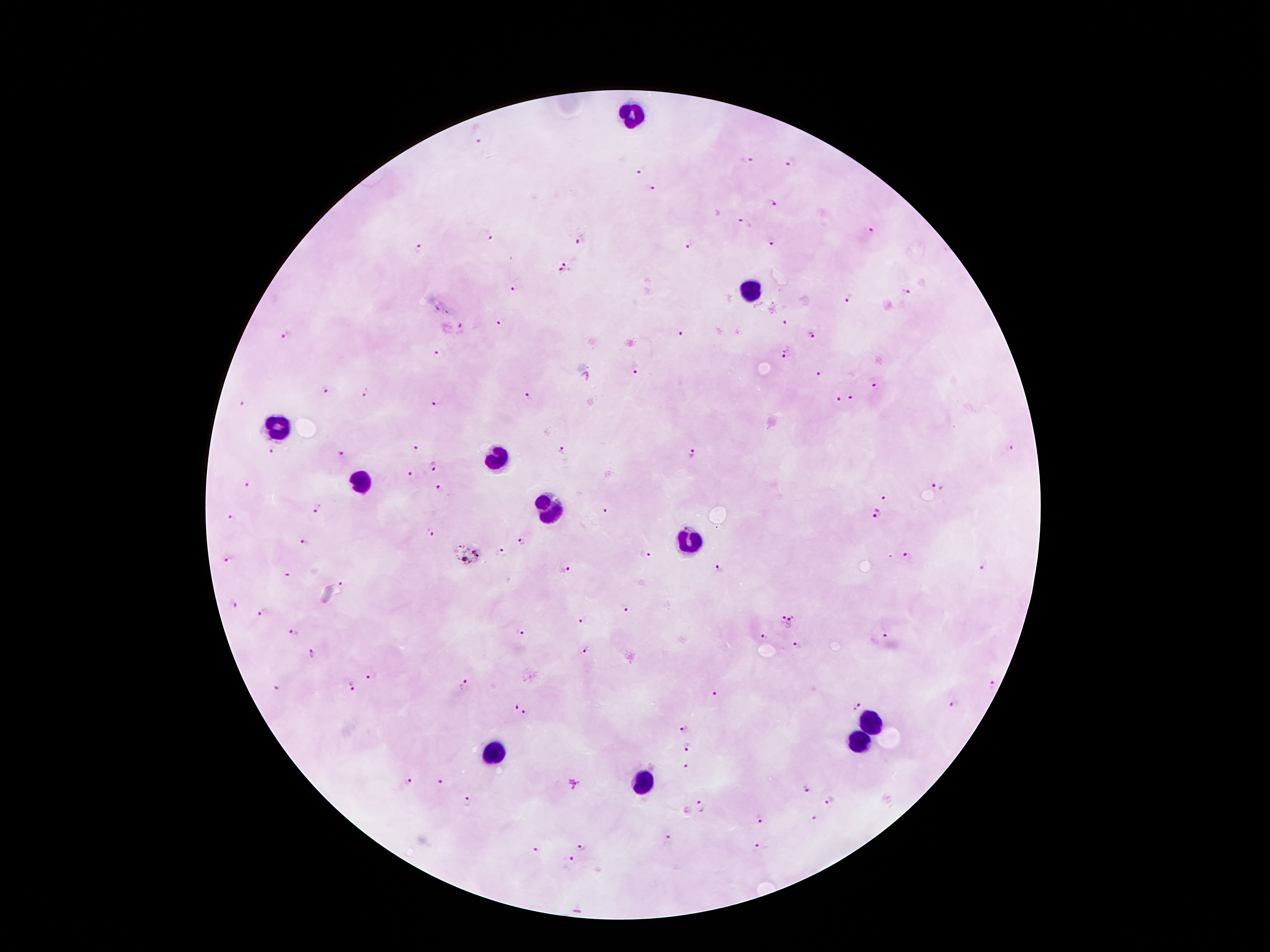

Approximate centers as [x, y] in pixels.
Summary:
  - Plasmodium parasite locations: [480, 142], [746, 161], [793, 162], [642, 170], [652, 189], [774, 203], [745, 224], [870, 230], [581, 239], [490, 240], [771, 241], [691, 245], [418, 248], [566, 262], [560, 273], [516, 288], [906, 293], [850, 301], [502, 322], [783, 323], [461, 326], [680, 333], [286, 336], [811, 336], [435, 352], [787, 353], [636, 368], [821, 376], [874, 385], [326, 387], [365, 393], [529, 396], [852, 397], [839, 401], [435, 402], [242, 404], [417, 447], [1012, 448], [271, 451], [561, 452], [341, 454], [692, 454], [433, 467], [410, 474], [249, 485], [935, 486], [440, 488], [883, 498], [319, 509], [604, 511], [877, 512], [234, 517], [432, 531], [521, 540], [306, 542], [501, 552], [646, 552], [909, 555], [228, 558], [985, 567], [566, 568], [720, 569], [289, 576], [344, 584], [236, 605], [627, 609], [264, 612], [779, 619], [581, 620], [794, 623], [293, 633], [521, 633], [765, 636], [887, 637], [798, 646], [587, 650], [311, 652], [369, 677], [464, 685], [992, 685], [352, 686], [278, 688], [713, 694], [515, 705], [953, 705], [855, 706], [525, 715], [684, 730], [686, 746], [686, 765], [409, 781], [443, 782], [574, 784], [806, 789], [831, 799], [469, 802], [700, 808], [813, 819], [760, 821], [670, 840], [582, 847], [760, 849], [534, 852], [572, 860]
  - Leukocyte locations: [634, 115], [753, 292], [276, 429], [499, 460], [364, 486], [548, 508], [686, 540], [868, 722], [860, 743], [493, 753], [639, 784]
  - Stain: Giemsa
  - Image size: 1270×952 pixels
  - Field of view: single
  - Preparation: thick blood smear
  - Capture: smartphone camera through the microscope eyepiece
  - Patient malaria status: positive for Plasmodium falciparum
  - Magnification: 100x